Comment on the morphology of the erythrocytes.
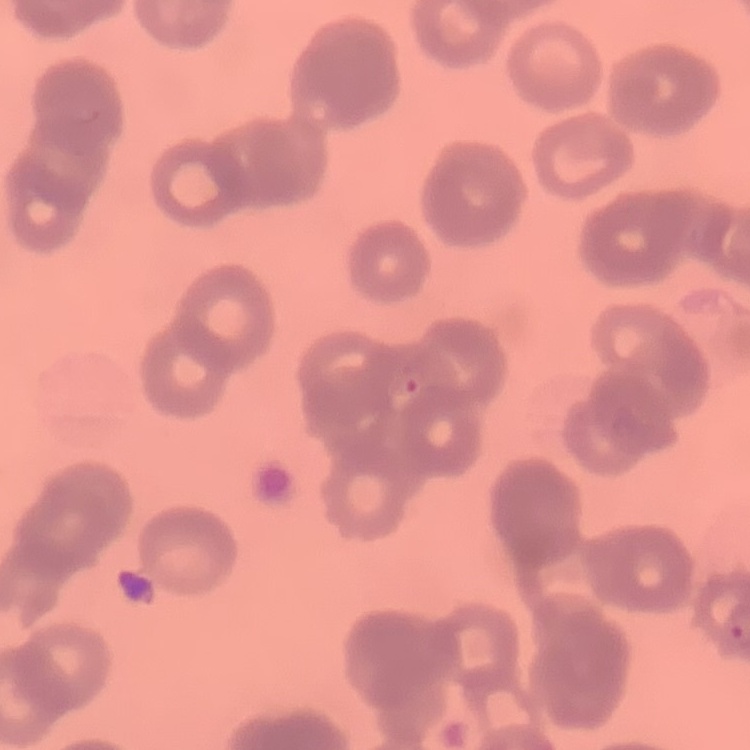

Rouleaux formation.

stain = Field's or Giemsa
preparation = thin blood smear
image type = square crop of a larger photomicrograph